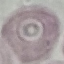
{
  "malaria_status": "uninfected",
  "capture": "smartphone camera at the microscope eyepiece",
  "preparation": "thin smear",
  "image_type": "automatically extracted cell patch, resized to 64 × 64 pixels",
  "stain": "Giemsa"
}